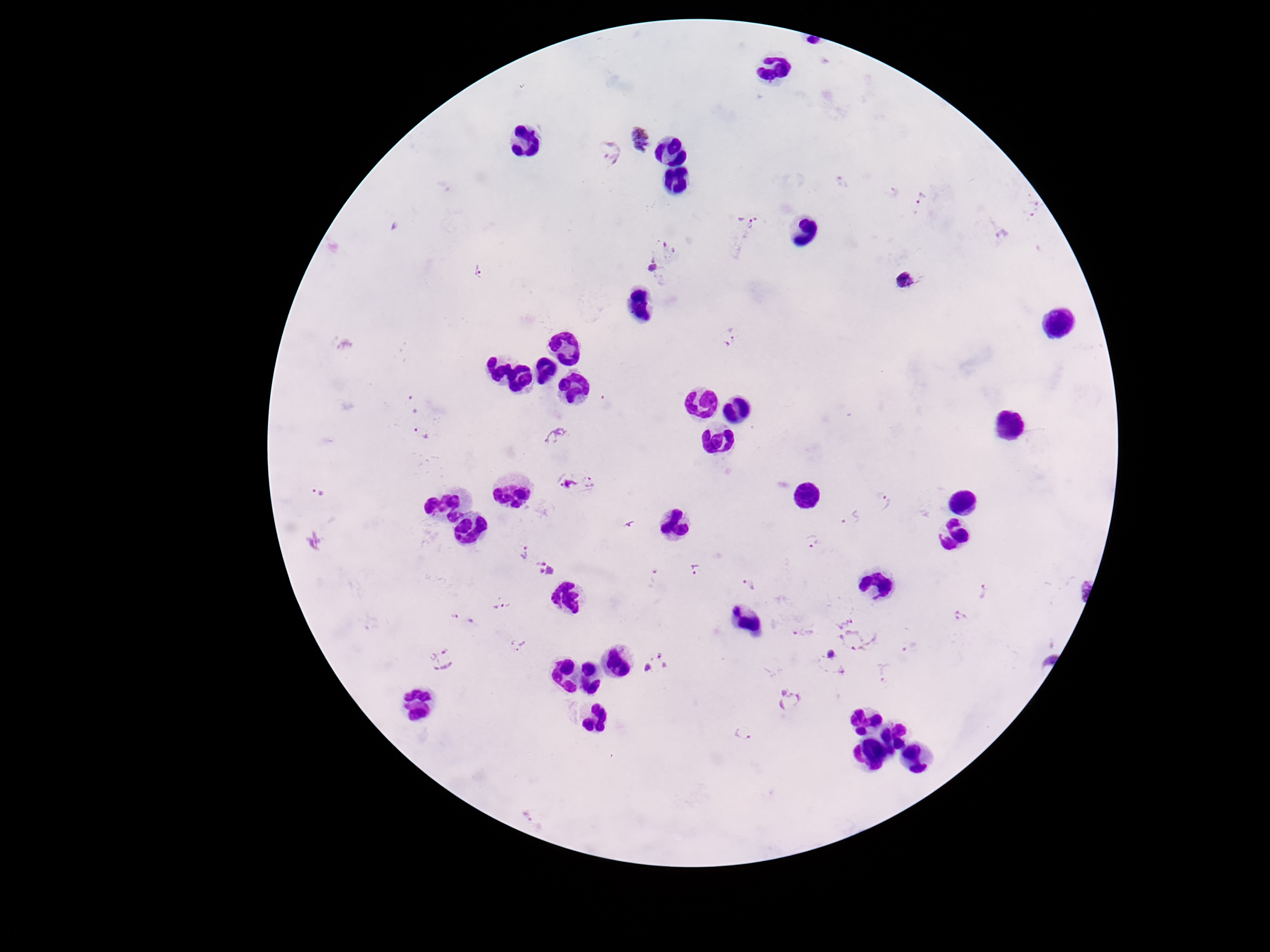
preparation: thick blood film
field_of_view: one from this slide
patient_malaria_status: positive
stain: Giemsa
plasmodium_parasite_locations: 'approximate centers as (x, y) in pixels: (640, 141), (608, 154), (843, 183), (892, 192), (922, 199), (1031, 208), (747, 222), (1001, 234), (670, 247), (651, 267), (480, 273), (906, 280), (731, 337), (413, 404), (421, 434), (557, 435), (587, 482), (564, 484), (315, 495), (885, 504), (850, 518), (628, 526), (316, 540), (812, 541), (523, 552), (547, 569), (696, 569), (655, 577), (1080, 585), (749, 587), (983, 592), (501, 604), (961, 616), (464, 619), (842, 620), (803, 634), (858, 637), (518, 644), (910, 647), (442, 660), (831, 664), (656, 665), (885, 672), (789, 701), (742, 733), (532, 818)'
capture: smartphone camera through the microscope eyepiece
image_size: 1270×952 pixels
magnification: 100x